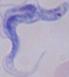
Photomicrograph. A trypanosome is seen. 1000x magnification.